Describe the morphology of the erythrocytes.
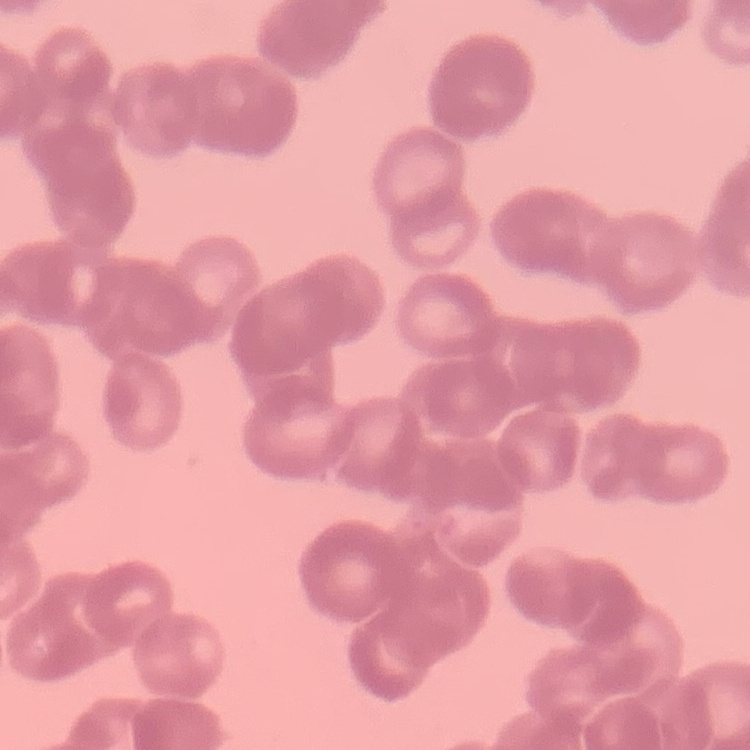

Rouleaux formation.

Field's or Giemsa stain. Square crop of a larger photomicrograph. Thin blood film.